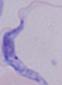
Summary:
  - Identification: trypanosome
  - Modality: micrograph
  - Magnification: 1000x